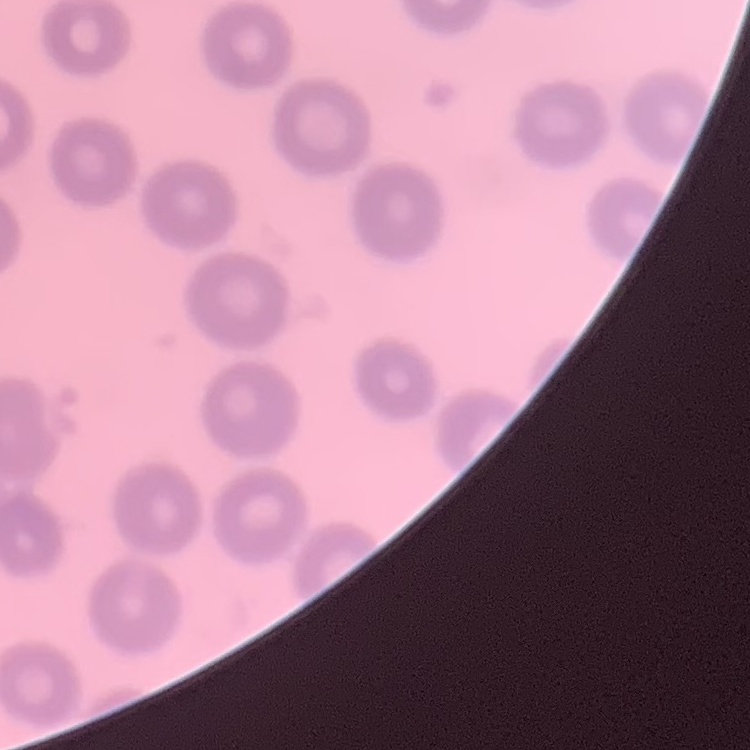

Summary:
  - Erythrocyte morphology: no rouleaux formation
  - Preparation: thin blood smear
  - Stain: Field's or Giemsa
  - Image type: one tile cut from a larger photomicrograph